Name the parasite shown.
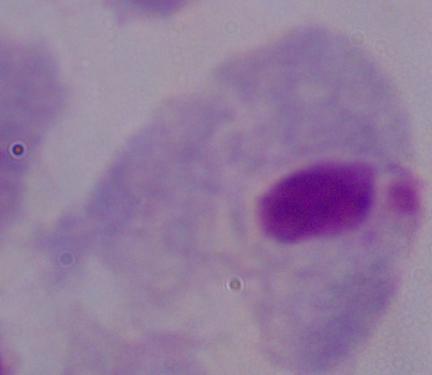

This is a trichomonad.

Photomicrograph. 1000x magnification.